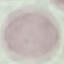

Summary:
  - Result: no malaria parasites detected
  - Preparation: thin blood smear
  - Stain: Giemsa
  - Image type: automatically extracted cell patch, resized to 64 × 64 pixels
  - Capture: smartphone through the microscope eyepiece